Name the blood parasite species.
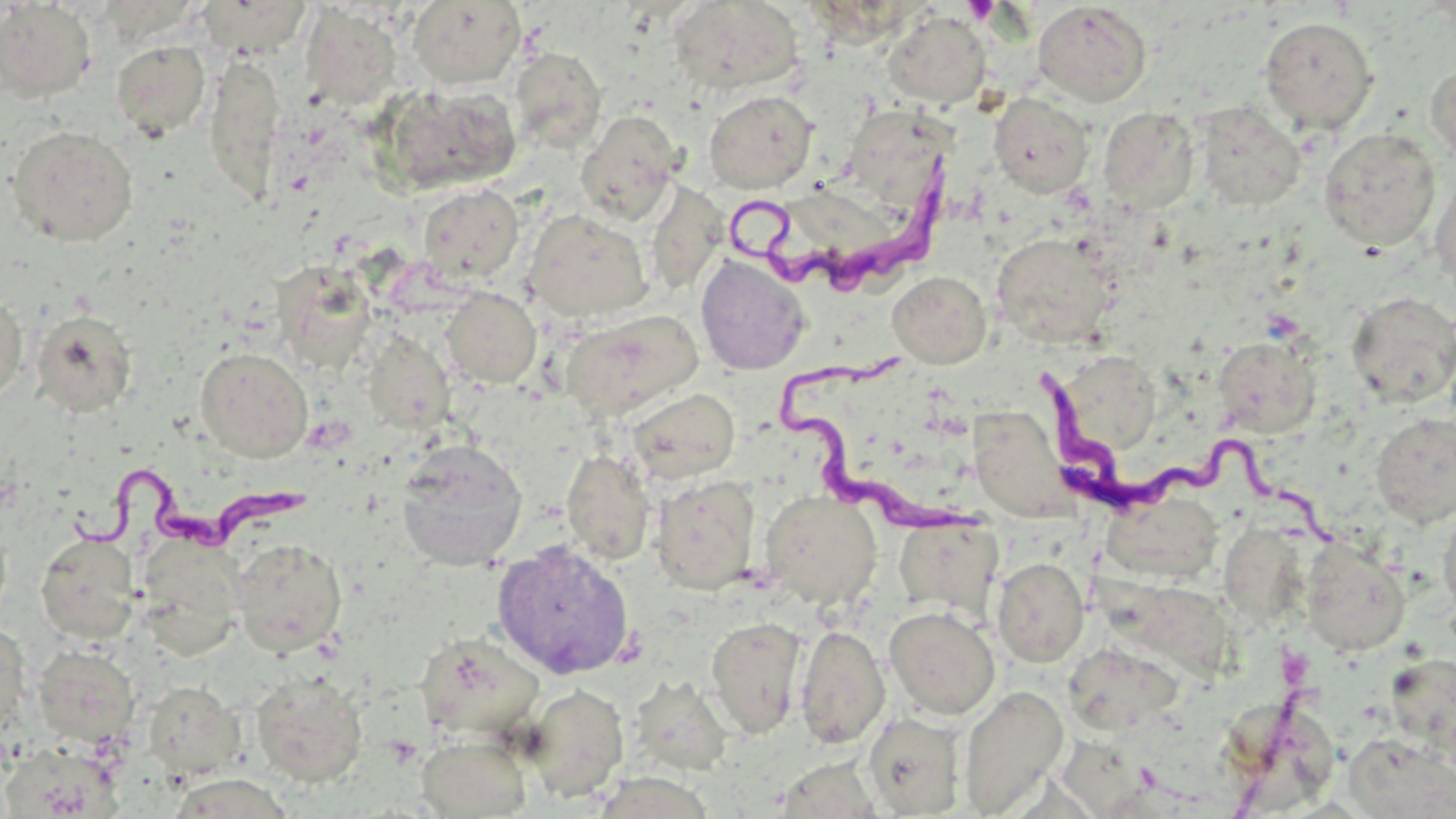

Trypanosoma brucei.

preparation = thin blood smear
uninfected red blood cell locations = approximate bounding boxes as (x1,y1)-(x2,y2) corner pairs in pixels: (667,0)-(805,96), (197,1)-(312,56), (408,1)-(525,88), (0,2)-(96,102), (1032,2)-(1152,107), (301,5)-(402,109), (883,11)-(990,109), (1258,17)-(1378,133), (111,39)-(210,139), (510,46)-(606,155), (203,51)-(286,205), (1425,62)-(1456,168), (384,84)-(523,194), (704,90)-(818,194), (989,93)-(1094,197), (1193,102)-(1306,211), (841,105)-(954,211), (1097,106)-(1200,214), (576,110)-(683,226), (6,125)-(138,246), (1317,128)-(1441,251), (1432,169)-(1456,296), (644,179)-(726,296), (417,183)-(524,284), (780,185)-(886,259), (525,210)-(652,322), (990,233)-(1119,348), (695,254)-(811,375), (271,262)-(378,372), (887,271)-(992,368), (442,287)-(541,387), (1346,291)-(1456,408), (0,292)-(28,406), (560,308)-(703,422), (32,310)-(137,417), (363,330)-(455,433), (1212,336)-(1322,438), (195,347)-(313,463), (1070,362)-(1173,450), (627,388)-(740,485), (965,409)-(1086,537), (1370,413)-(1456,526), (395,440)-(528,571), (561,449)-(656,565), (650,475)-(760,595), (760,490)-(882,609), (1100,492)-(1223,584), (1438,497)-(1456,622), (895,516)-(1003,621), (36,533)-(141,644), (136,533)-(247,657), (1239,537)-(1310,627), (1299,537)-(1410,655), (230,538)-(347,657), (492,541)-(635,681), (992,557)-(1090,667), (1090,577)-(1241,690), (884,606)-(1000,719), (706,617)-(808,738), (0,619)-(30,737), (795,623)-(890,749), (415,631)-(546,740), (33,644)-(139,745), (1067,651)-(1180,741), (1385,651)-(1456,758), (250,671)-(368,786), (630,676)-(732,777), (143,681)-(244,779), (521,683)-(629,801), (958,685)-(1069,816), (1221,699)-(1333,805), (864,713)-(966,817), (1344,733)-(1455,818), (417,734)-(531,818), (1,741)-(122,817), (782,750)-(874,818), (584,767)-(720,817), (170,782)-(295,819)
Trypanosoma brucei locations = approximate bounding boxes as (x1,y1)-(x2,y2) corner pairs in pixels: (724,153)-(972,290), (774,349)-(993,550), (1026,369)-(1341,552), (67,456)-(316,564)
platelet locations = approximate bounding boxes as (x1,y1)-(x2,y2) corner pairs in pixels: (963,0)-(999,24)
field of view = single
image size = 1456×819 pixels
magnification = 1000x
modality = light microscopy
stain = May-Grünwald-Giemsa